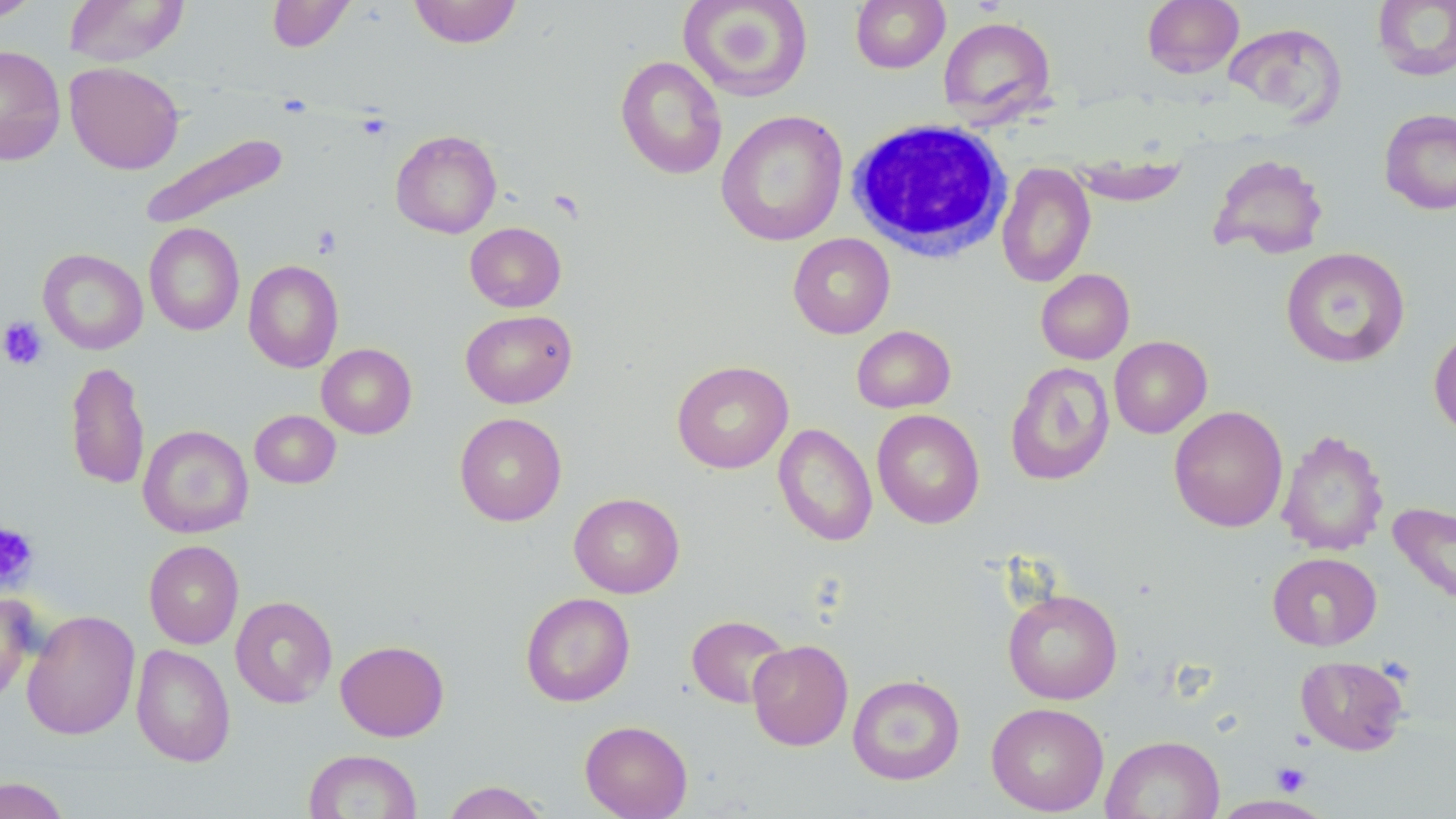
slide-level diagnosis = no evidence of blood parasites
white blood cell locations = approximate bounding boxes as named x1/y1/x2/y2 corners in pixels: (x1=845, y1=117, x2=1013, y2=262)
modality = optical microscopy
field of view = single
preparation = thin blood smear
uninfected red blood cell locations = approximate bounding boxes as named x1/y1/x2/y2 corners in pixels: (x1=0, y1=0, x2=39, y2=23), (x1=63, y1=0, x2=189, y2=67), (x1=267, y1=0, x2=356, y2=52), (x1=409, y1=0, x2=523, y2=49), (x1=678, y1=0, x2=813, y2=102), (x1=850, y1=0, x2=950, y2=73), (x1=1142, y1=0, x2=1244, y2=79), (x1=1372, y1=0, x2=1456, y2=82), (x1=938, y1=16, x2=1056, y2=125), (x1=1225, y1=23, x2=1345, y2=123), (x1=0, y1=45, x2=66, y2=166), (x1=616, y1=55, x2=728, y2=179), (x1=65, y1=61, x2=184, y2=174), (x1=1378, y1=108, x2=1456, y2=215), (x1=715, y1=110, x2=848, y2=246), (x1=390, y1=130, x2=501, y2=238), (x1=140, y1=132, x2=290, y2=230), (x1=1208, y1=153, x2=1330, y2=260), (x1=1069, y1=155, x2=1188, y2=206), (x1=996, y1=161, x2=1096, y2=288), (x1=144, y1=222, x2=245, y2=336), (x1=465, y1=222, x2=566, y2=312), (x1=788, y1=233, x2=895, y2=339), (x1=1281, y1=247, x2=1410, y2=368), (x1=38, y1=248, x2=147, y2=355), (x1=243, y1=260, x2=344, y2=372), (x1=1036, y1=268, x2=1134, y2=364), (x1=460, y1=310, x2=577, y2=408), (x1=1429, y1=324, x2=1456, y2=437), (x1=851, y1=325, x2=956, y2=413), (x1=1109, y1=336, x2=1212, y2=438), (x1=316, y1=343, x2=417, y2=439), (x1=65, y1=360, x2=149, y2=490), (x1=671, y1=360, x2=793, y2=474), (x1=1005, y1=361, x2=1115, y2=486), (x1=1169, y1=405, x2=1288, y2=533), (x1=871, y1=408, x2=985, y2=529), (x1=250, y1=409, x2=341, y2=488), (x1=454, y1=412, x2=567, y2=526), (x1=773, y1=423, x2=877, y2=546), (x1=138, y1=425, x2=253, y2=539), (x1=1276, y1=429, x2=1389, y2=556), (x1=569, y1=492, x2=685, y2=598), (x1=1389, y1=502, x2=1456, y2=610), (x1=144, y1=540, x2=243, y2=649), (x1=1267, y1=552, x2=1382, y2=650), (x1=1002, y1=587, x2=1123, y2=704), (x1=0, y1=592, x2=36, y2=704), (x1=520, y1=592, x2=635, y2=706), (x1=230, y1=596, x2=337, y2=708), (x1=22, y1=610, x2=140, y2=741), (x1=686, y1=613, x2=792, y2=709), (x1=335, y1=639, x2=449, y2=741), (x1=747, y1=639, x2=853, y2=751), (x1=131, y1=644, x2=235, y2=766), (x1=1296, y1=655, x2=1410, y2=755), (x1=847, y1=674, x2=965, y2=785), (x1=986, y1=702, x2=1109, y2=816), (x1=580, y1=720, x2=693, y2=819), (x1=1101, y1=735, x2=1224, y2=819), (x1=303, y1=749, x2=422, y2=818), (x1=0, y1=777, x2=70, y2=819), (x1=440, y1=781, x2=551, y2=818), (x1=1211, y1=794, x2=1330, y2=818)
image size = 1456×819 pixels
magnification = 1000x
stain = May-Grünwald-Giemsa
platelet locations = approximate bounding boxes as named x1/y1/x2/y2 corners in pixels: (x1=311, y1=225, x2=343, y2=258), (x1=0, y1=316, x2=48, y2=370), (x1=0, y1=522, x2=38, y2=589), (x1=1273, y1=763, x2=1308, y2=795)